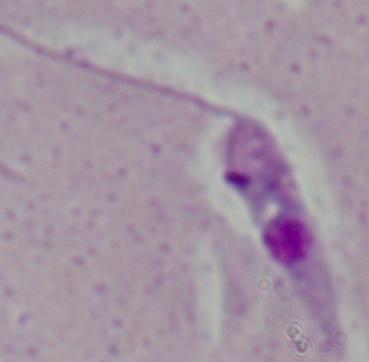 A Leishmania parasite is seen. 1000x magnification. Photomicrograph.